Outline platelets.
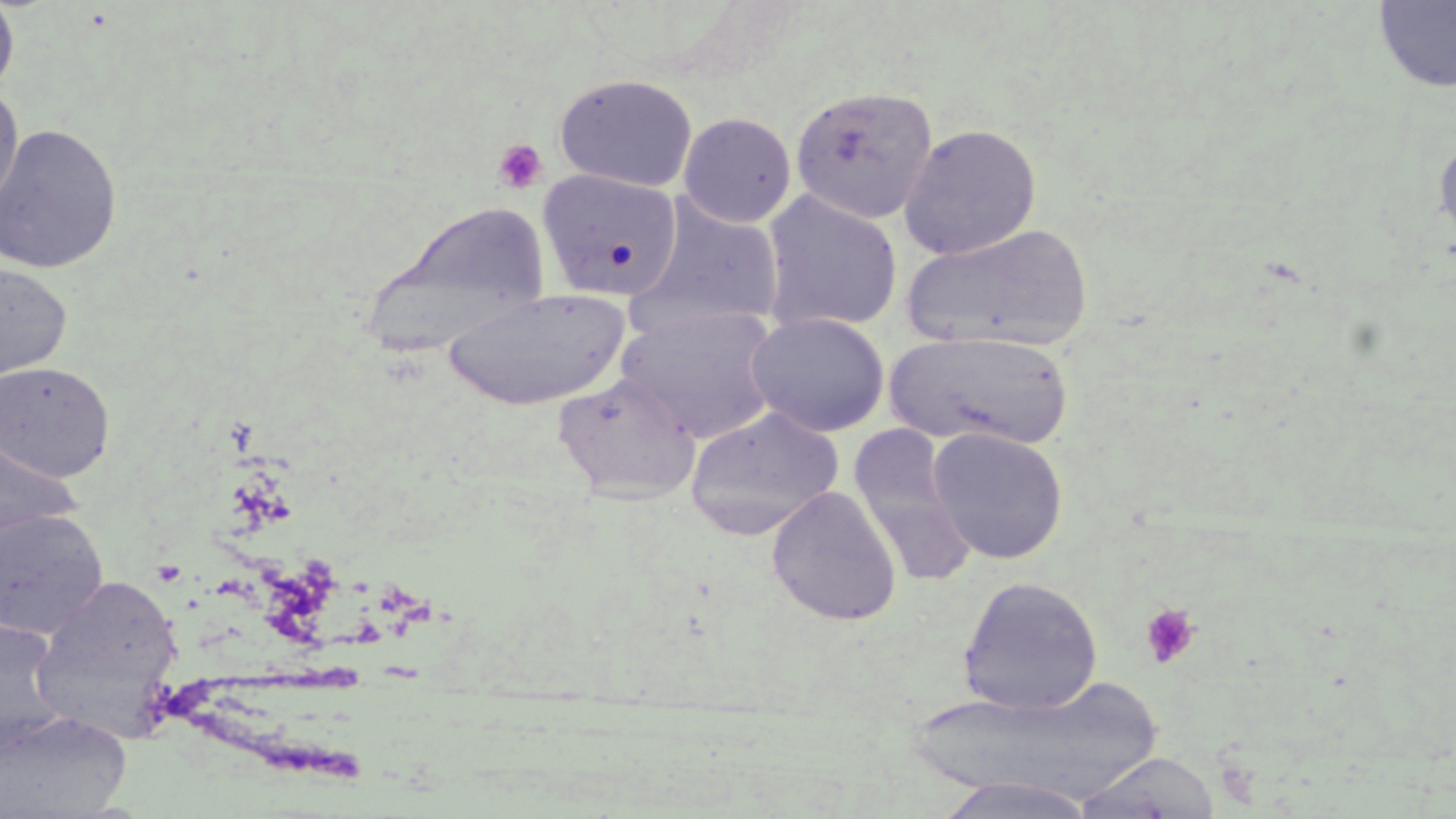

Approximate bounding boxes as (x1,y1)-(x2,y2) corner pairs in pixels.
Platelets: (492,138)-(549,194), (1139,603)-(1201,669).

Summary:
  - Uninfected red blood cell locations: (0,0)-(19,100), (1373,0)-(1456,95), (554,73)-(699,193), (789,85)-(939,224), (0,87)-(23,216), (678,112)-(797,228), (0,122)-(122,275), (898,123)-(1042,260), (1432,131)-(1456,252), (536,168)-(684,303), (760,190)-(902,334), (633,198)-(786,333), (364,199)-(551,357), (903,223)-(1094,352), (0,263)-(72,385), (442,287)-(631,410), (618,304)-(783,443), (746,312)-(890,436), (884,329)-(1076,450), (0,361)-(115,482), (553,372)-(703,504), (685,406)-(844,540), (848,425)-(979,589), (927,426)-(1068,565), (0,434)-(81,546), (767,486)-(902,626), (0,509)-(109,639), (31,574)-(185,730), (958,576)-(1103,715), (0,618)-(71,757), (908,676)-(1171,808), (0,710)-(131,817), (1071,750)-(1222,818), (932,776)-(1101,819)
  - Slide-level diagnosis: no evidence of blood parasites
  - Stain: May-Grünwald-Giemsa
  - Preparation: thin blood smear
  - Field of view: single
  - Image size: 1456×819 pixels
  - Modality: optical microscopy
  - Magnification: 1000x